Assess this cell for malaria.
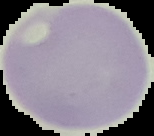

Uninfected.

image size = 154×136 pixels
image type = cell region segmented out of the field of view; surrounding area masked to black
preparation = thin blood film